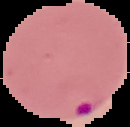
image type = segmented cell region on a black background
image size = 130×127 pixels
malaria status = parasitized
preparation = thin blood film